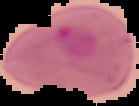

Summary:
  - Image size: 139×106 pixels
  - Image type: segmented cell region with the area outside set to black
  - Malaria status: parasitized
  - Preparation: thin blood smear